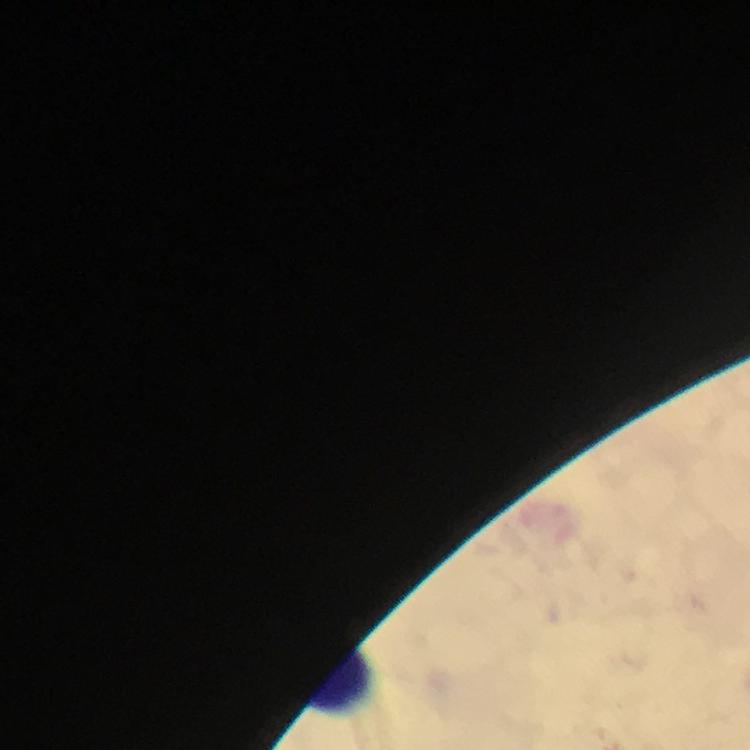

Approximate object centers, in pixels from the top-left corner.
Summary:
  - Leukocyte locations: (x=338, y=676)
  - Capture: smartphone mounted on the microscope
  - Context: from a diagnostic examination for malaria
  - Cropped from: one field of view
  - Plasmodium parasites: none seen
  - Stain: Giemsa
  - Preparation: thick smear
  - Immersion oil: used
  - Image size: 750×750 pixels
  - Magnification: 100x